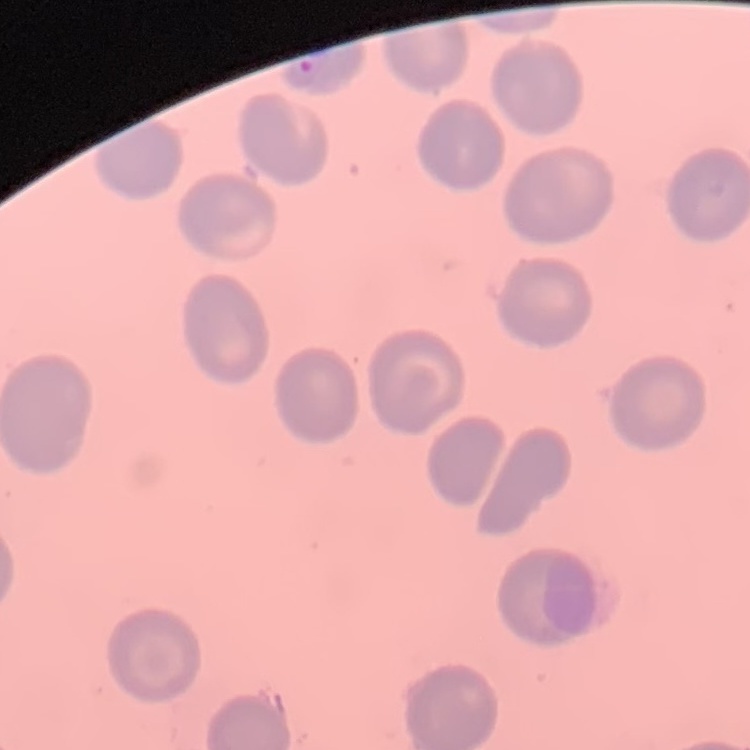
Summary:
  - Red blood cell morphology: no rouleaux formation
  - Image type: one tile cut from a larger photomicrograph
  - Preparation: thin peripheral smear
  - Stain: Field's or Giemsa